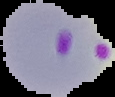
Result: Plasmodium parasites identified. Image is 115×97 pixels. From a thin blood smear. The area outside the segmented cell region is set to black.